State the preparation type.
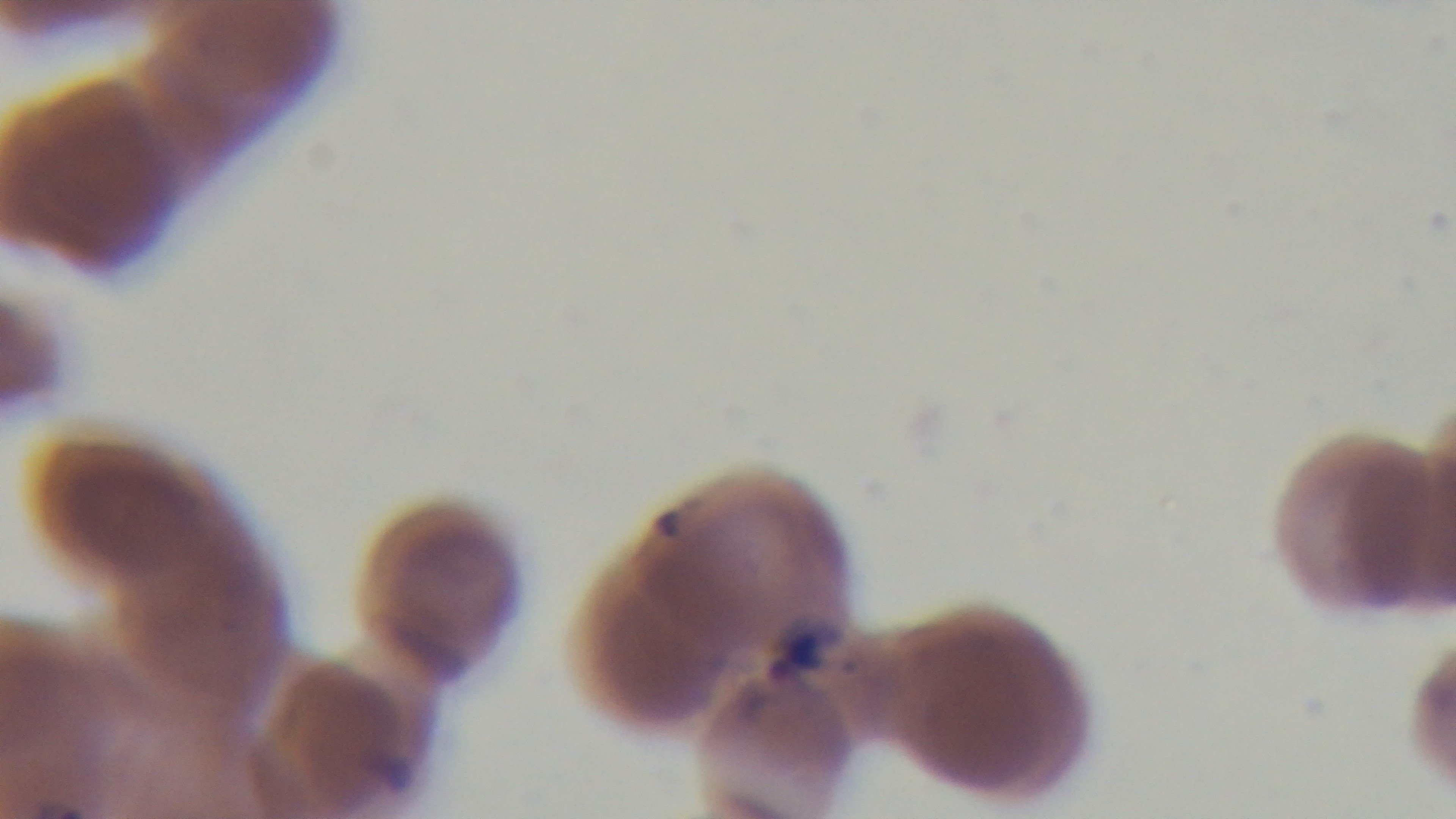
A thin smear.

objective = 100x oil immersion
field of view = single
capture = mounted 4K digital camera
malaria status = infected
stain = Giemsa
modality = light microscopy